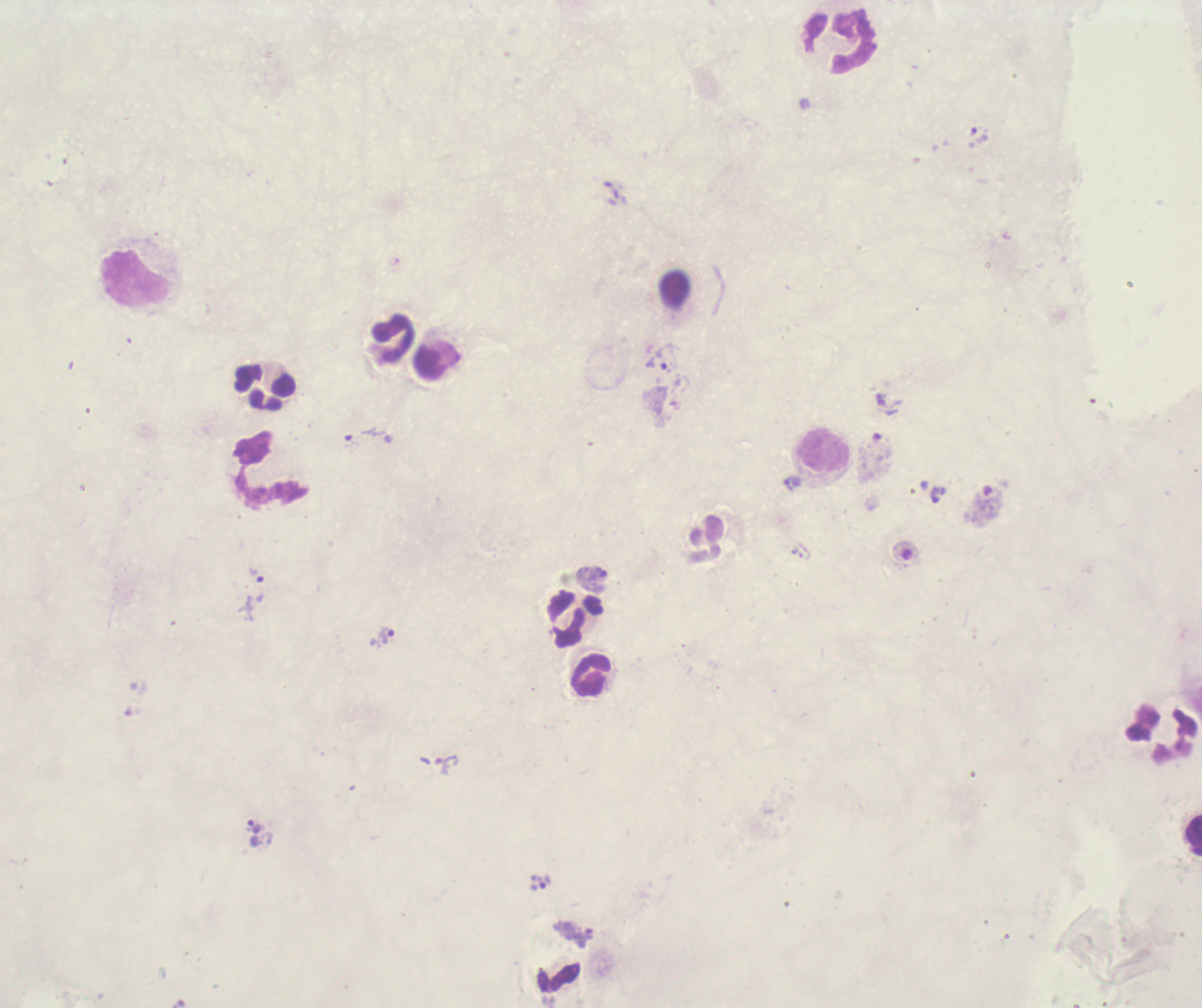
image_size: 1202×1008 pixels
stain: Romanowsky
leukocyte_locations: 'approximate centers as [x, y] in pixels: [840, 42], [138, 279], [393, 339], [266, 388], [825, 450], [271, 470], [578, 620], [592, 675], [1193, 834]'
background_quality: poor
magnification: 100x
coloration_quality: bad
preparation: thick blood smear
result: positive for Plasmodium parasites
context: previously used in an actual diagnosis
field_of_view: single
trophozoite_locations: 'approximate centers as [x, y] in pixels: [979, 136], [658, 362], [364, 436], [793, 484], [938, 496], [257, 575], [382, 637], [255, 828], [540, 883]'